Outline platelets.
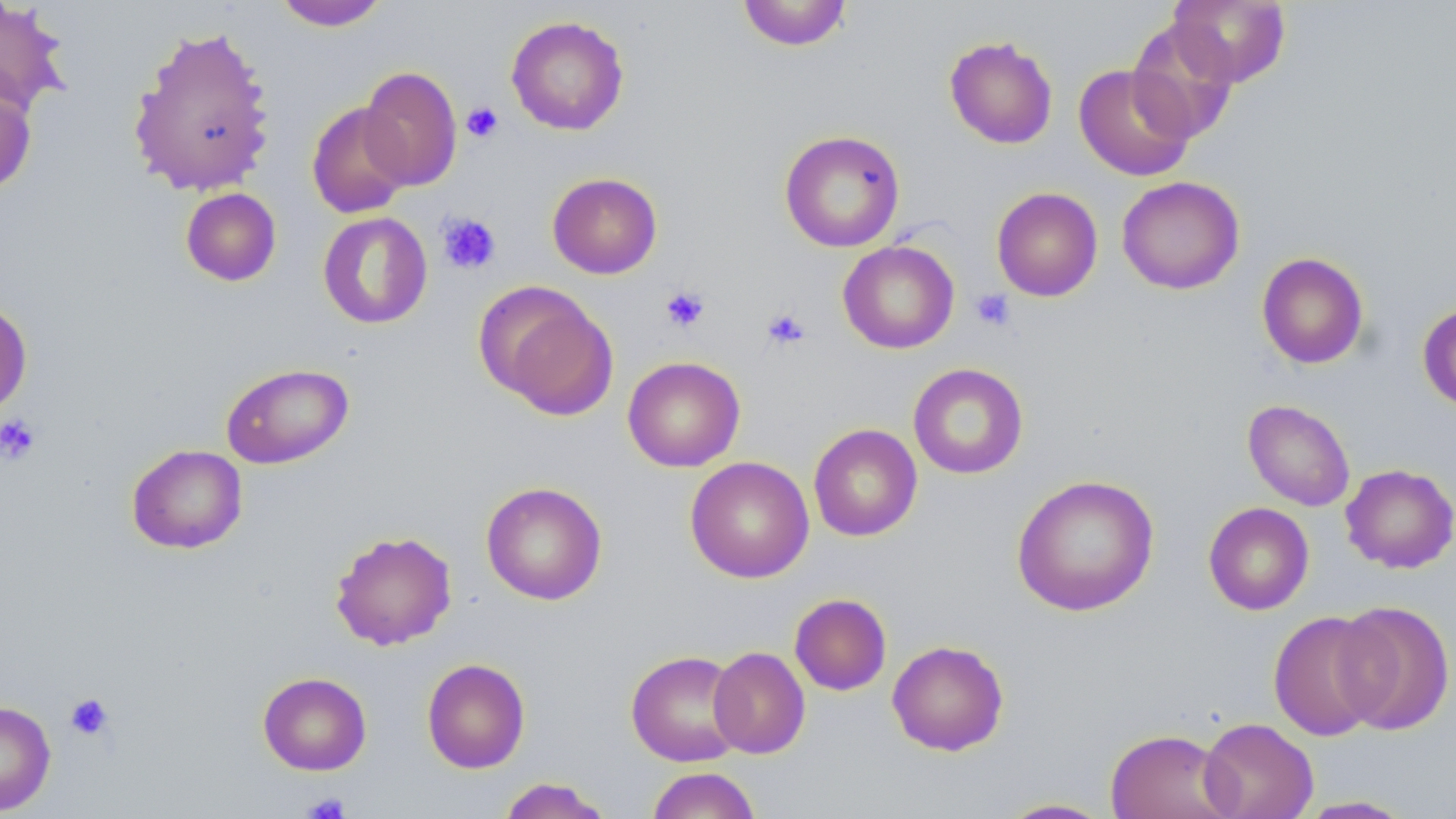
Approximate bounding boxes as (x1, y1, x2, y2) in pixels.
Platelets: (461, 102, 503, 143), (437, 213, 501, 275), (660, 285, 710, 333), (970, 288, 1016, 332), (761, 307, 810, 351), (0, 414, 41, 466), (63, 692, 115, 741), (302, 792, 352, 819).

Uninfected red blood cell locations: (273, 0, 390, 31), (736, 0, 853, 51), (1168, 0, 1292, 87), (0, 2, 71, 117), (506, 15, 630, 135), (1126, 19, 1239, 144), (126, 22, 276, 198), (943, 35, 1058, 149), (1073, 64, 1196, 182), (358, 66, 462, 191), (0, 84, 37, 195), (306, 102, 413, 219), (779, 130, 905, 252), (547, 172, 662, 279), (1116, 175, 1245, 295), (180, 187, 282, 287), (991, 187, 1103, 302), (318, 212, 433, 329), (838, 240, 960, 354), (1256, 252, 1369, 369), (476, 282, 617, 418), (0, 297, 33, 419), (1417, 301, 1456, 413), (623, 356, 745, 472), (221, 362, 354, 469), (908, 362, 1029, 479), (1243, 399, 1356, 511), (808, 423, 923, 542), (126, 444, 248, 554), (685, 456, 814, 583), (1340, 463, 1456, 574), (1011, 474, 1160, 617), (481, 481, 608, 605), (1203, 502, 1314, 615), (329, 529, 457, 651), (789, 593, 892, 696), (1333, 600, 1455, 735), (1268, 611, 1388, 742), (887, 639, 1009, 756), (708, 646, 810, 759), (626, 649, 745, 767), (422, 658, 530, 773), (257, 671, 372, 775), (0, 700, 56, 815), (1198, 717, 1318, 819), (1105, 728, 1238, 819), (646, 767, 761, 819), (496, 777, 615, 819), (1294, 796, 1417, 818), (996, 797, 1116, 818). Slide-level diagnosis: no evidence of blood parasites. May-Grünwald-Giemsa stain. Image is 1456×819 pixels. 1000x magnification. One field of a larger specimen. Light microscopy. Thin blood smear.